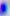
Summary:
  - Identification: Toxoplasma gondii
  - Magnification: 400x
  - Modality: micrograph